Identify the parasite.
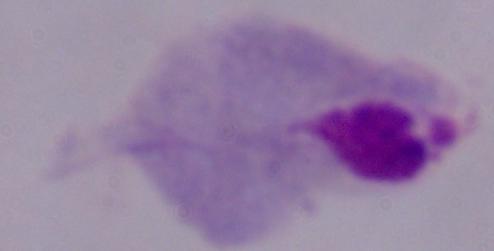
This is a trichomonad.

modality = photomicrograph
magnification = 1000x